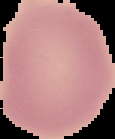

preparation = thin blood film
malaria status = uninfected
image type = cell region segmented out of the field of view; surrounding area masked to black
image size = 115×139 pixels